Classify this cell by malaria status.
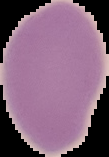
Uninfected.

preparation = thin blood smear
image size = 109×157 pixels
image type = cell region segmented out of the field of view; surrounding area masked to black